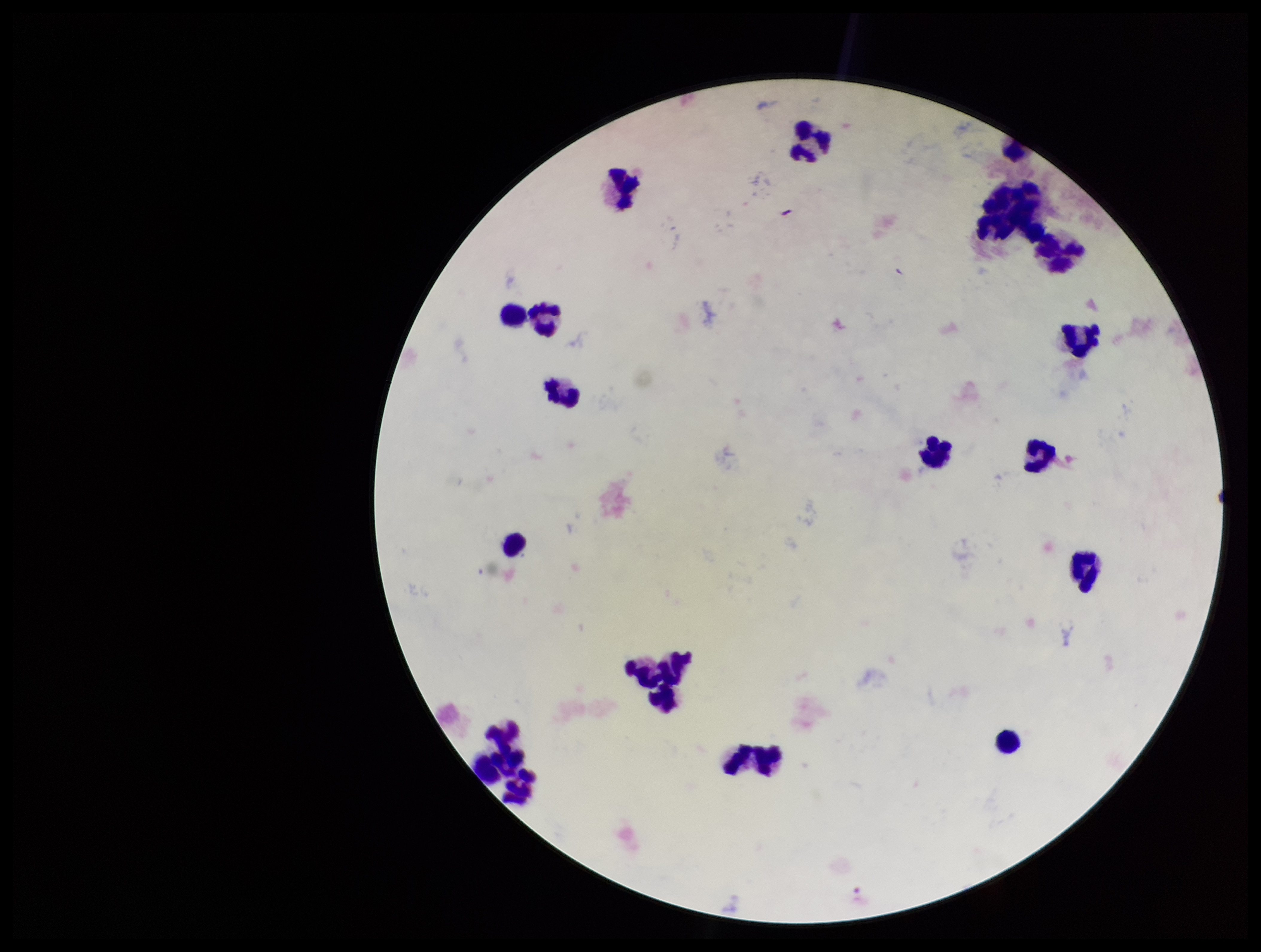
Summary:
  - Image size: 1261×952 pixels
  - Preparation: thick smear
  - Plasmodium parasites: none seen
  - Leukocyte count: 19
  - Stain: Giemsa
  - Capture: smartphone photograph through the microscope eyepiece
  - Patient malaria status: negative
  - Parasite count: 0
  - Field of view: single